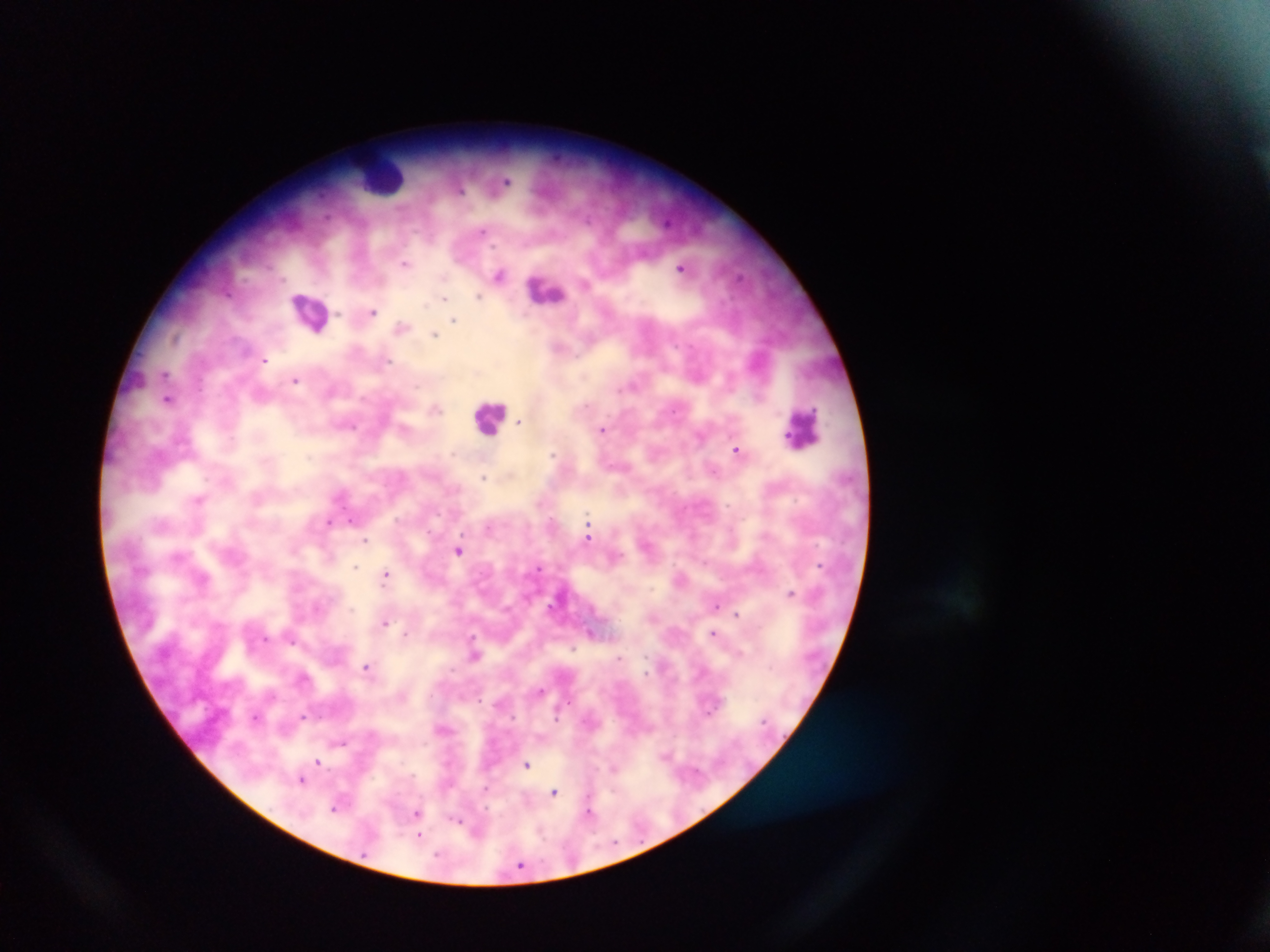

Approximate centers as (x, y) in pixels.
Summary:
  - Leukocyte locations: (382, 176), (546, 290), (311, 311), (130, 382), (490, 416), (803, 426)
  - Plasmodium parasite locations: (508, 181), (460, 190), (483, 231), (405, 263), (681, 267), (500, 274), (478, 296), (445, 298), (373, 311), (453, 320), (401, 327), (434, 335), (175, 337), (264, 361), (385, 361), (166, 373), (295, 380), (168, 399), (436, 409), (674, 410), (518, 422), (353, 427), (602, 429), (736, 449), (553, 454), (483, 477), (199, 500), (588, 518), (352, 520), (329, 522), (589, 538), (366, 540), (459, 551), (819, 565), (355, 567), (539, 567), (385, 575), (791, 592), (551, 605), (716, 606), (737, 614), (385, 622), (592, 633), (712, 633), (406, 634), (472, 638), (291, 640), (573, 648), (739, 652), (475, 655), (619, 658), (366, 667), (646, 672), (541, 690), (303, 716), (256, 717), (342, 743), (666, 755), (317, 761), (526, 765), (613, 768), (301, 780), (554, 792), (335, 807), (589, 812), (417, 813), (457, 821), (419, 836), (520, 865)
  - Preparation: thick blood film
  - Country: Ghana
  - Field of view: single
  - Image size: 1270×952 pixels
  - Capture: mobile-phone photograph through a microscope